Assess the morphology of the red blood cells.
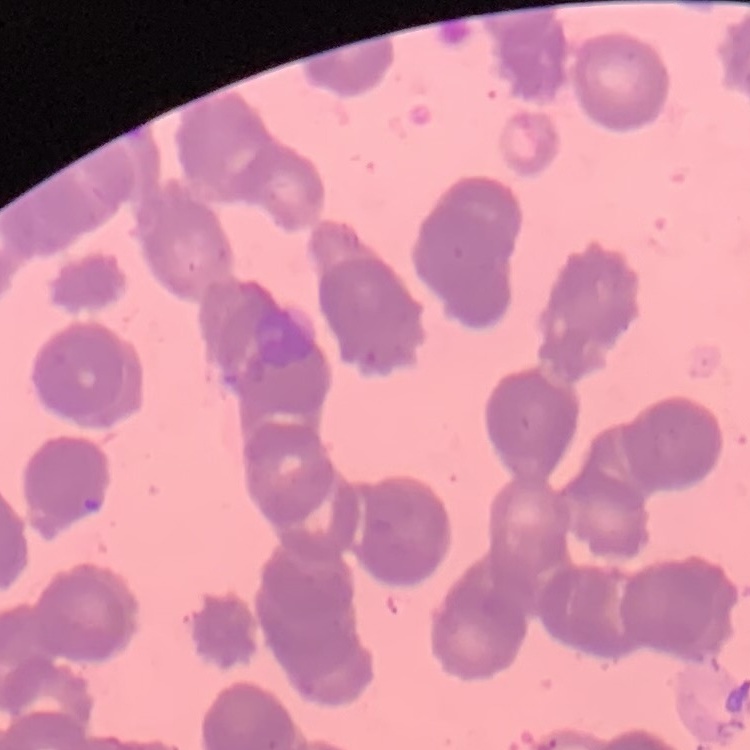

They show rouleaux formation.

Summary:
  - Image type: square crop of a larger photomicrograph
  - Preparation: thin blood film
  - Stain: Field's or Giemsa